Point out each malaria parasite.
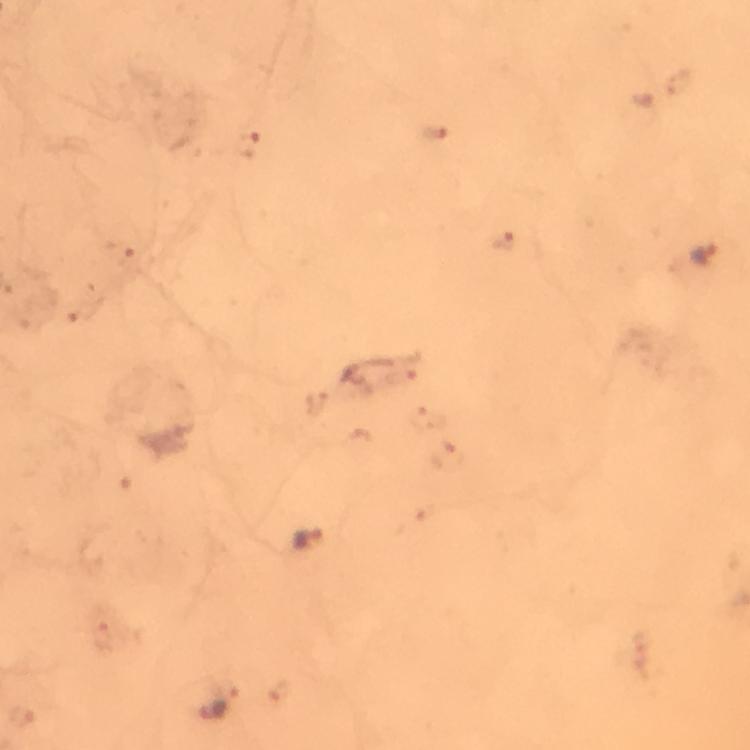
Approximate centers as {x, y} in pixels.
Malaria parasites: {704, 253}, {305, 538}, {213, 709}.

Immersion oil applied. Cropped region of a single field of view. Thick smear. Image is 750×750 pixels. Giemsa-stained preparation. 100x magnification. Photographed with a smartphone mounted on the microscope. From a malaria diagnostic workup.